Assess this cell for malaria.
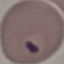

It is parasitized.

preparation = thin blood film
stain = Giemsa
image type = cell patch, automatically extracted from a larger field of view and resized to 64 × 64 pixels
capture = smartphone camera at the microscope eyepiece